Identify the parasite.
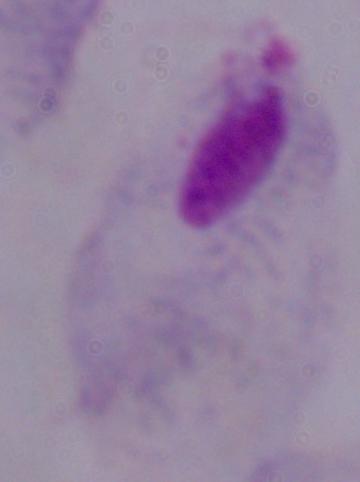
A trichomonad.

Captured at 1000x magnification. Photomicrograph.